Identify the parasite.
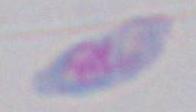

Toxoplasma gondii.

Photomicrograph. Captured at 1000x magnification.